Name the cell type shown.
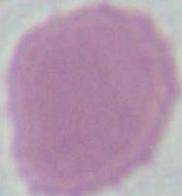
This is an erythrocyte.

modality = micrograph
magnification = 1000x